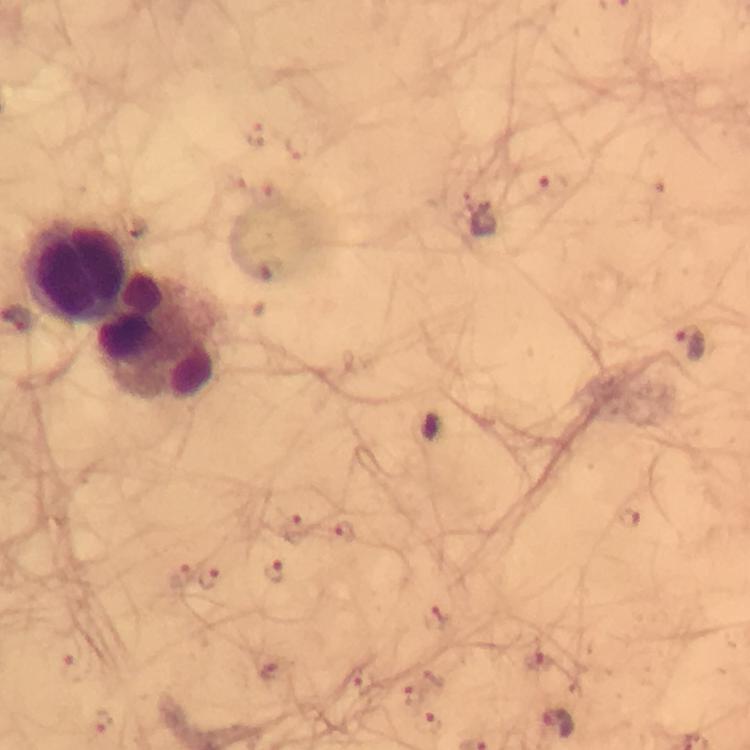

Approximate centers as [x, y] in pixels.
Summary:
  - Leukocyte locations: [80, 272], [163, 337]
  - Plasmodium parasite locations: [550, 185], [484, 221], [691, 343], [631, 518], [296, 529], [345, 531], [277, 571], [182, 575], [209, 577], [434, 620], [536, 659], [79, 667], [365, 683], [415, 694], [104, 721], [431, 723], [560, 725]
  - Context: from a diagnostic examination for malaria
  - Cropped from: a single field of view
  - Image size: 750×750 pixels
  - Stain: Giemsa
  - Capture: smartphone photograph through a microscope
  - Magnification: 100x
  - Immersion oil: used
  - Preparation: thick smear